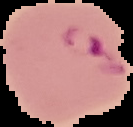 Malaria status: parasitized. Image is 133×127 pixels. Cell region segmented out of the field of view; the surrounding area is masked to black. From a thin blood smear.